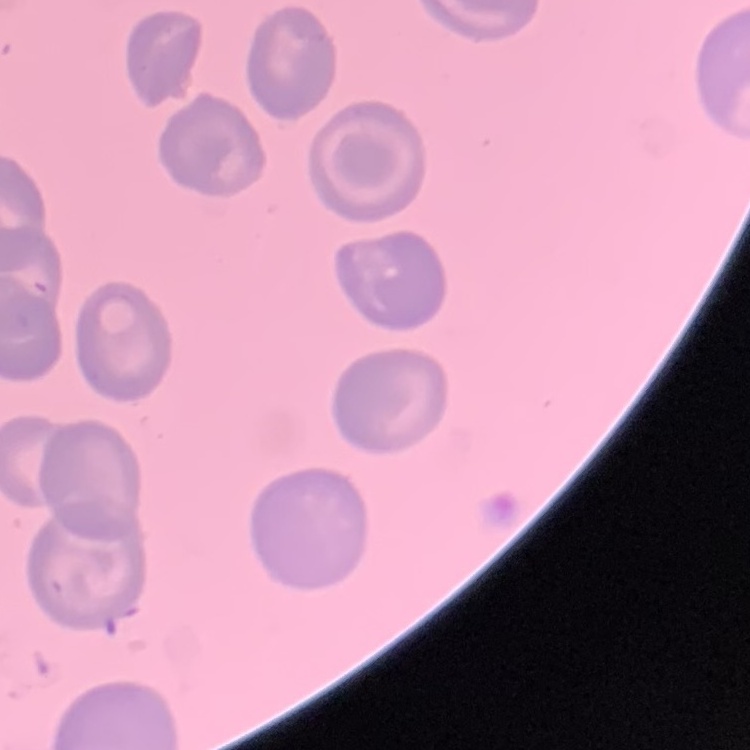
{
  "red_blood_cell_morphology": "no rouleaux formation",
  "image_type": "square crop of a larger photomicrograph",
  "preparation": "thin blood smear",
  "stain": "Field's or Giemsa"
}